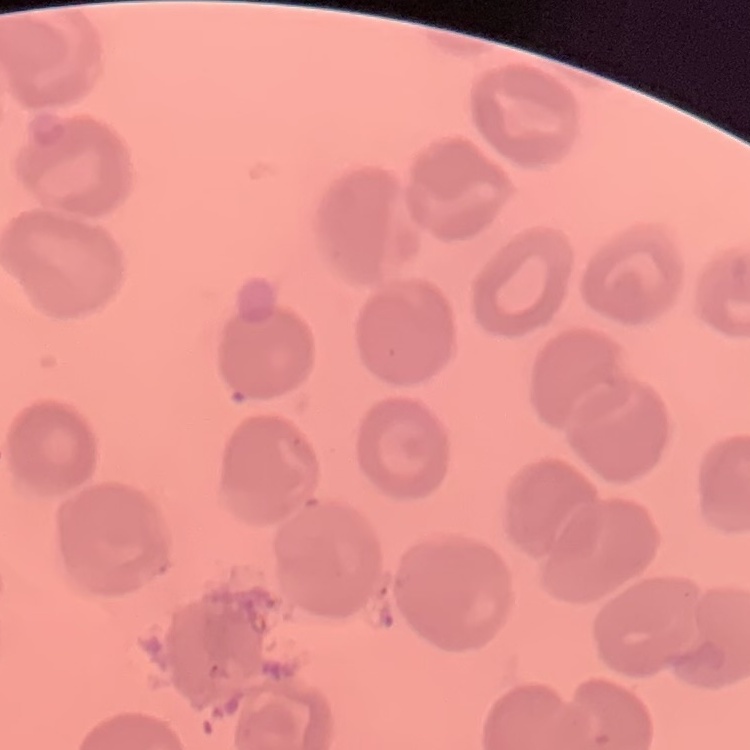

red_blood_cell_morphology: no rouleaux formation
image_type: one tile cut from a larger photomicrograph
preparation: thin peripheral smear
stain: Field's or Giemsa